Locate platelets.
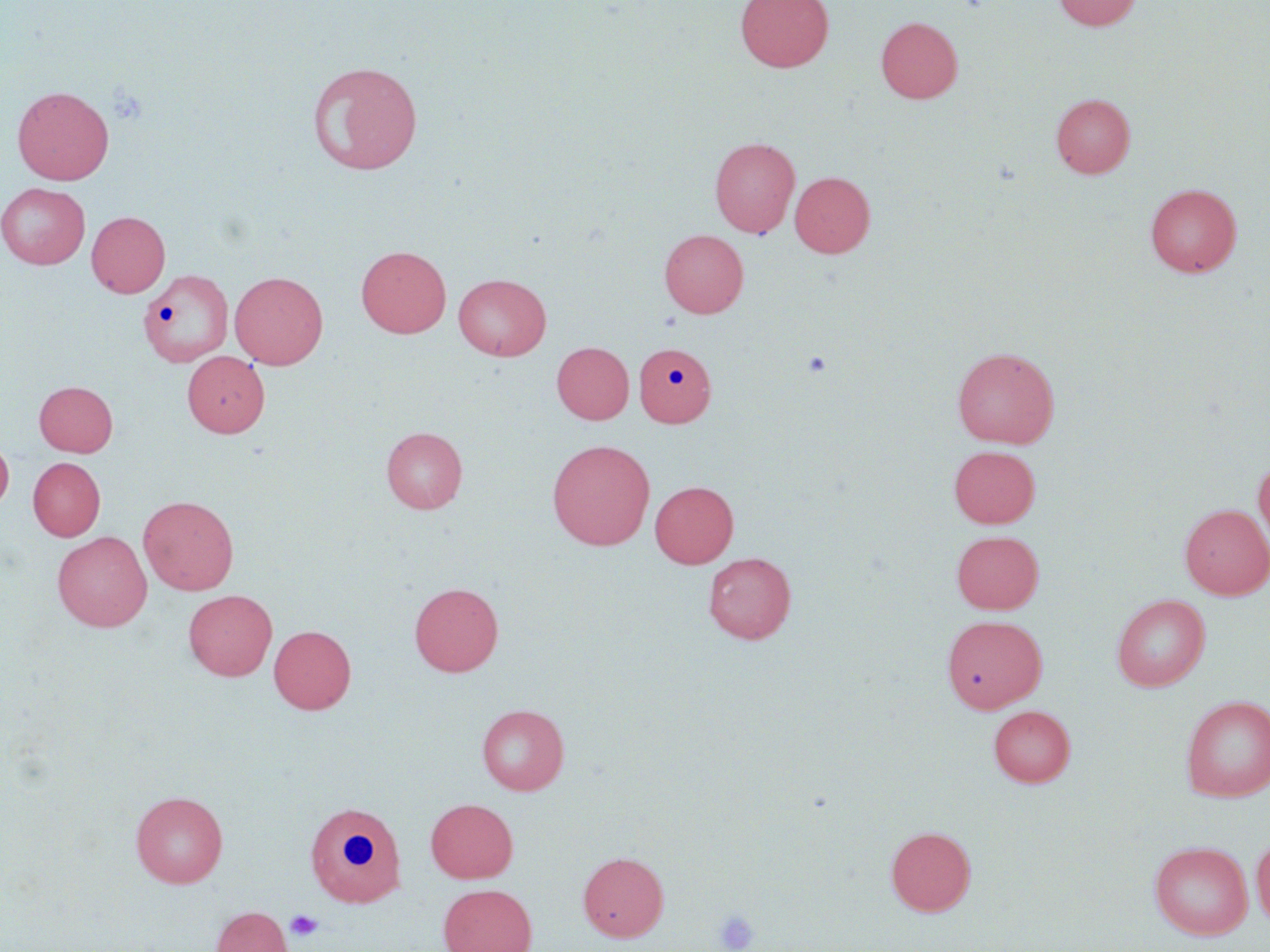
Approximate bounding boxes as [x1, y1, x2, y2] in pixels.
Platelets: [801, 350, 832, 377], [714, 908, 761, 951], [285, 909, 323, 942].

slide-level diagnosis = no evidence of blood parasites
modality = light microscopy
preparation = thin blood smear
field of view = one of a larger specimen
magnification = 1000x
stain = May-Grünwald-Giemsa
image size = 1270×952 pixels
uninfected red blood cell locations = approximate bounding boxes as [x1, y1, x2, y2] in pixels: [736, 0, 833, 71], [1053, 0, 1143, 31], [876, 16, 962, 103], [307, 60, 424, 176], [12, 86, 114, 184], [1051, 93, 1135, 178], [709, 136, 800, 238], [789, 171, 875, 258], [0, 182, 90, 269], [1145, 183, 1242, 277], [87, 211, 170, 297], [659, 229, 748, 318], [356, 246, 451, 338], [142, 270, 236, 368], [229, 271, 328, 369], [453, 273, 551, 360], [552, 342, 634, 424], [634, 342, 716, 427], [952, 346, 1060, 448], [182, 351, 269, 437], [34, 381, 117, 457], [381, 426, 467, 513], [0, 437, 13, 514], [548, 439, 655, 549], [948, 445, 1040, 528], [1253, 455, 1270, 548], [28, 457, 105, 541], [649, 481, 738, 568], [138, 494, 239, 595], [1180, 504, 1270, 599], [951, 529, 1044, 614], [52, 531, 152, 632], [704, 552, 796, 643], [409, 582, 504, 676], [184, 589, 276, 681], [1111, 594, 1211, 691], [942, 615, 1047, 712], [269, 625, 356, 714], [1180, 695, 1270, 801], [477, 703, 570, 795], [988, 705, 1076, 787], [130, 790, 227, 888], [303, 798, 408, 908], [425, 798, 518, 883], [885, 826, 976, 916], [1251, 834, 1270, 929], [1149, 840, 1253, 940], [578, 851, 669, 941], [438, 883, 537, 952], [211, 906, 292, 952]